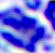 Photomicrograph. Captured at 400x magnification. A white blood cell is seen.